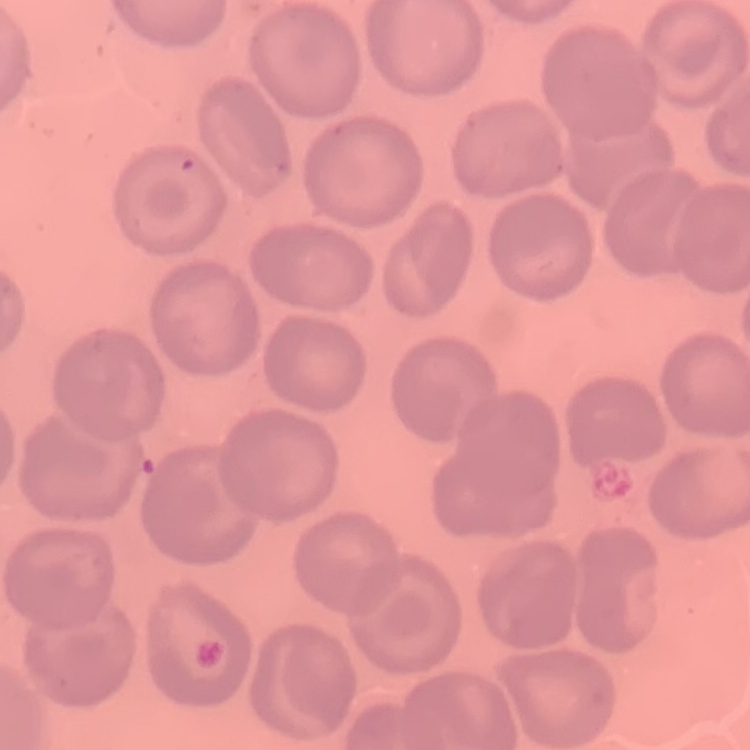
Summary:
  - Erythrocyte morphology: no rouleaux formation
  - Image type: square crop of a larger photomicrograph
  - Preparation: thin peripheral smear
  - Stain: Field's or Giemsa